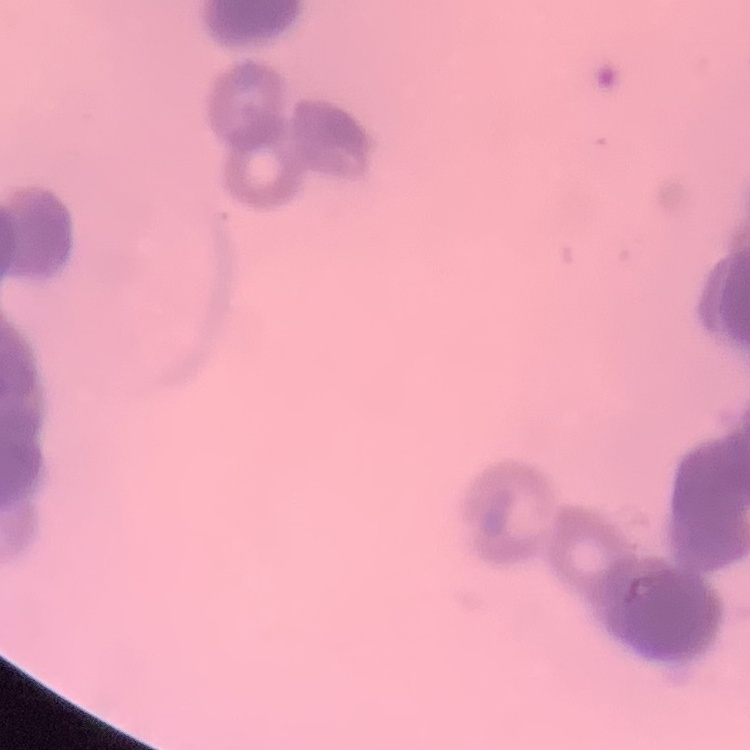
erythrocyte morphology = rouleaux formation
image type = square crop of a larger photomicrograph
preparation = thin blood film
stain = Field's or Giemsa